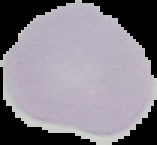
From a thin blood smear. Image is 157×145 pixels. Result: negative for Plasmodium parasites. Segmented cell region on a black background.